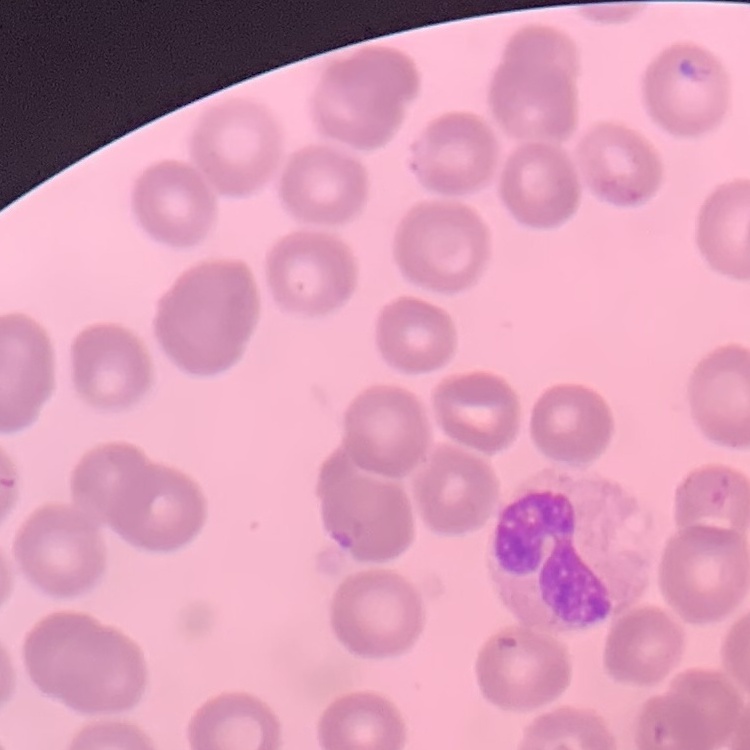

The erythrocytes exhibit no rouleaux formation. Thin peripheral smear. Square crop of a larger photomicrograph. Field's or Giemsa stain.